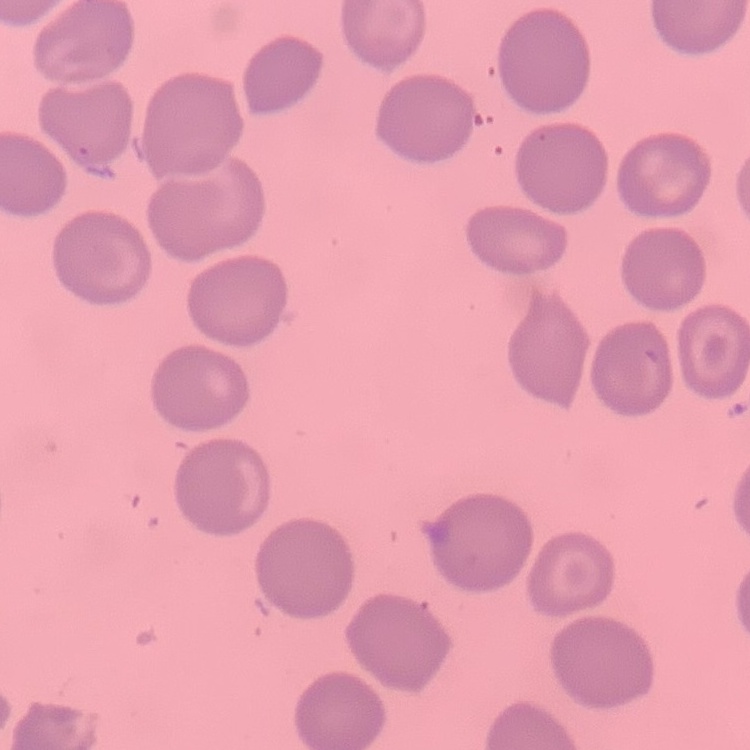

Summary:
  - Erythrocyte morphology: no rouleaux formation
  - Preparation: thin peripheral smear
  - Stain: Field's or Giemsa
  - Image type: one tile cut from a larger photomicrograph